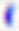

Summary:
  - Identification: Toxoplasma gondii
  - Magnification: 400x
  - Modality: photomicrograph